Classify this cell by malaria status.
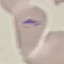

It is parasitized.

Giemsa stain. Cell patch, automatically extracted from a larger field of view and resized to 64 × 64 pixels. Thin blood film. Photographed with a smartphone camera at the microscope eyepiece.